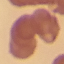
malaria status = uninfected
capture = smartphone camera at the microscope eyepiece
preparation = thin blood smear
stain = Giemsa
image type = automatically extracted cell patch, resized to 64 × 64 pixels